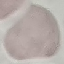
Summary:
  - Malaria status: uninfected
  - Image type: cell patch, automatically extracted from a larger field of view and resized to 64 × 64 pixels
  - Preparation: thin blood film
  - Capture: smartphone camera at the microscope eyepiece
  - Stain: Giemsa